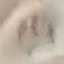

Summary:
  - Malaria status: uninfected
  - Capture: smartphone camera at the microscope eyepiece
  - Stain: Giemsa
  - Preparation: thin smear
  - Image type: automatically extracted cell patch, resized to 64 × 64 pixels